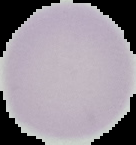
Result: no Plasmodium parasites seen. Segmented cell region on a black background. From a thin blood film. Image is 136×145 pixels.